Assess this cell for malaria.
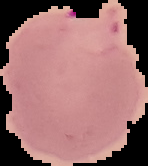
Parasitized.

Cell region segmented out of the field of view; the surrounding area is masked to black. From a thin blood smear. Image is 148×166 pixels.